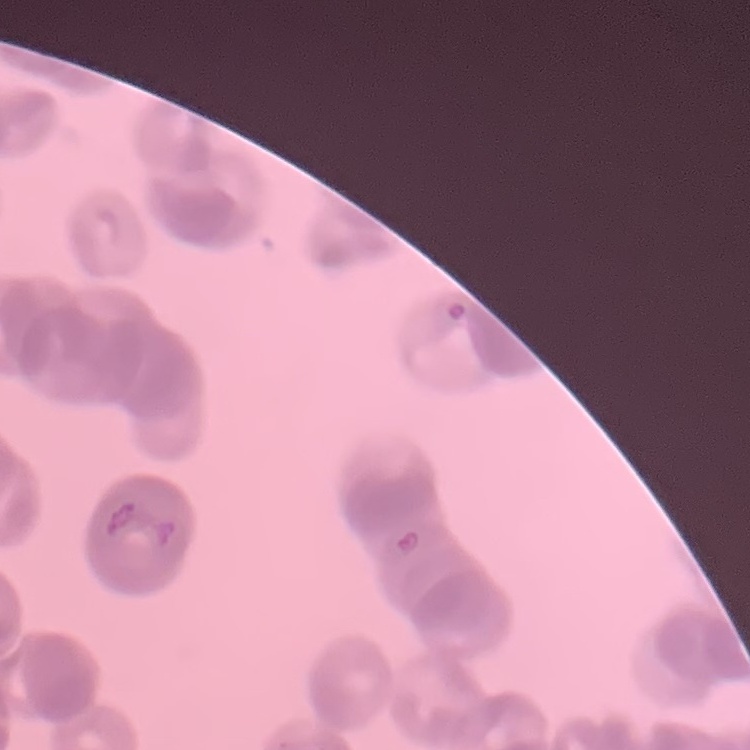

The red blood cells show rouleaux formation. Field's or Giemsa stain. Square crop of a larger photomicrograph. Thin blood film.